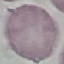 Result: no malaria parasites seen. Giemsa stain. Cell patch, automatically extracted from a larger field of view and resized to 64 × 64 pixels. Thin blood smear. Photographed with a smartphone camera at the microscope eyepiece.